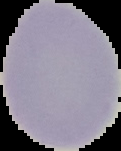
Summary:
  - Image type: cell region segmented out of the field of view; surrounding area masked to black
  - Image size: 121×151 pixels
  - Result: negative for malaria parasites
  - Preparation: thin blood film